Outline each Plasmodium ovale-infected red blood cell.
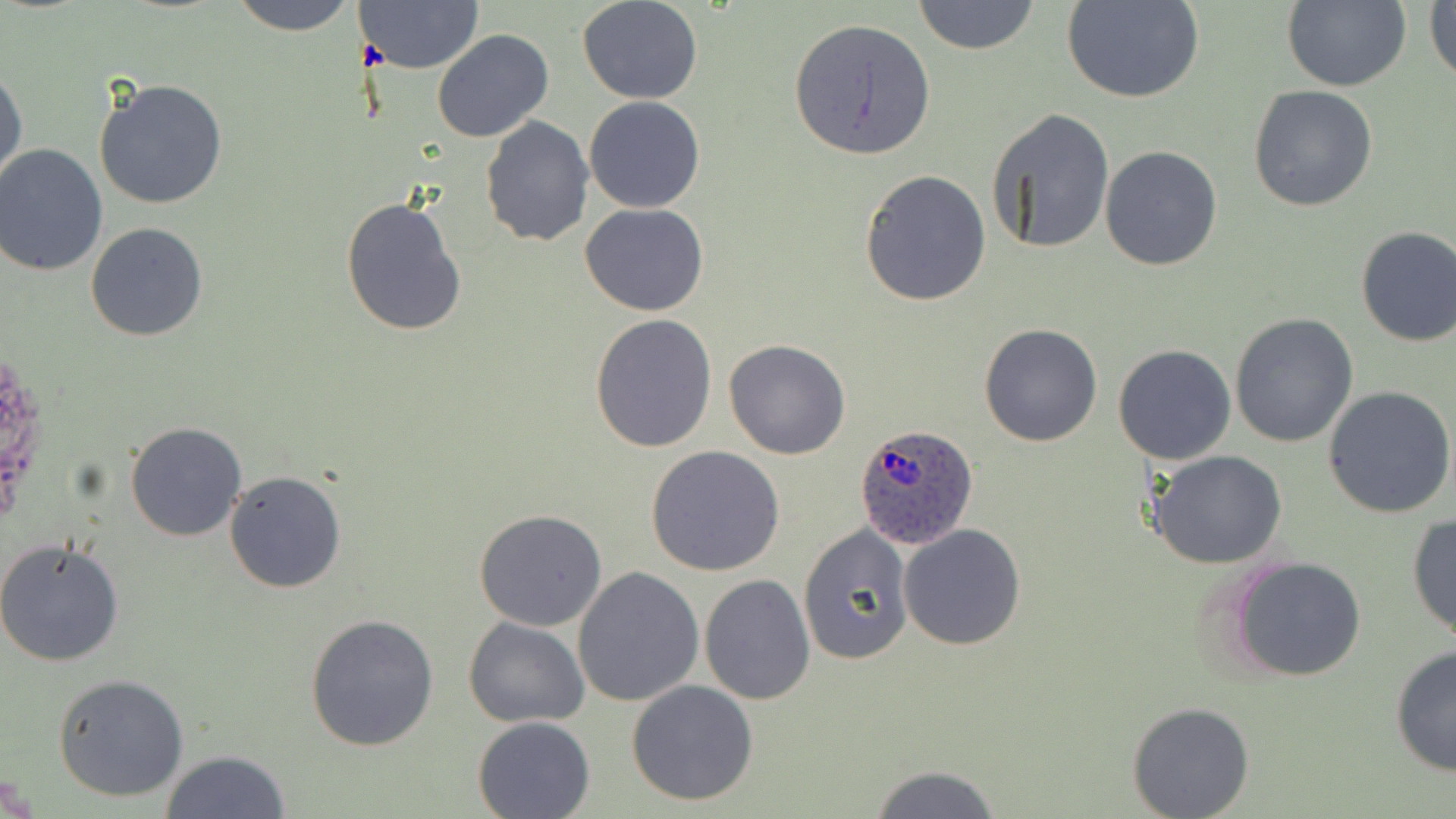

Approximate bounding boxes as [x1, y1, x2, y2] in pixels.
Plasmodium ovale-infected red blood cells: [853, 420, 979, 548].

Uninfected red blood cell locations: [229, 0, 359, 35], [356, 0, 485, 73], [577, 0, 703, 104], [912, 0, 1041, 56], [1062, 0, 1206, 105], [1426, 0, 1456, 90], [1280, 2, 1409, 89], [788, 17, 936, 161], [432, 29, 554, 142], [0, 67, 28, 188], [94, 79, 228, 210], [1248, 84, 1379, 213], [583, 95, 706, 213], [986, 109, 1115, 258], [479, 115, 594, 247], [0, 145, 108, 276], [1100, 145, 1223, 270], [859, 169, 991, 306], [339, 196, 468, 337], [580, 202, 708, 316], [85, 222, 208, 342], [1353, 225, 1456, 346], [588, 312, 718, 453], [1230, 312, 1360, 448], [978, 322, 1104, 447], [724, 338, 852, 459], [1113, 343, 1237, 465], [1323, 385, 1456, 519], [125, 421, 247, 542], [646, 445, 786, 577], [1149, 452, 1289, 571], [224, 471, 347, 593], [473, 508, 608, 631], [1408, 512, 1456, 641], [897, 523, 1027, 650], [798, 524, 914, 666], [0, 538, 125, 668], [1227, 555, 1366, 681], [574, 566, 705, 706], [700, 574, 815, 703], [306, 612, 440, 751], [463, 616, 589, 727], [1390, 644, 1456, 779], [52, 674, 190, 802], [627, 679, 760, 806], [1126, 701, 1255, 817], [472, 716, 594, 819], [161, 749, 293, 818], [865, 764, 1002, 819]. Slide-level diagnosis: Plasmodium ovale. May-Grünwald-Giemsa stain. Image is 1456×819 pixels. Optical microscopy. One field of a larger specimen. Captured at 1000x magnification. Thin blood film.